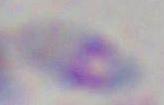

Summary:
  - Identification: Toxoplasma gondii
  - Magnification: 1000x
  - Modality: photomicrograph